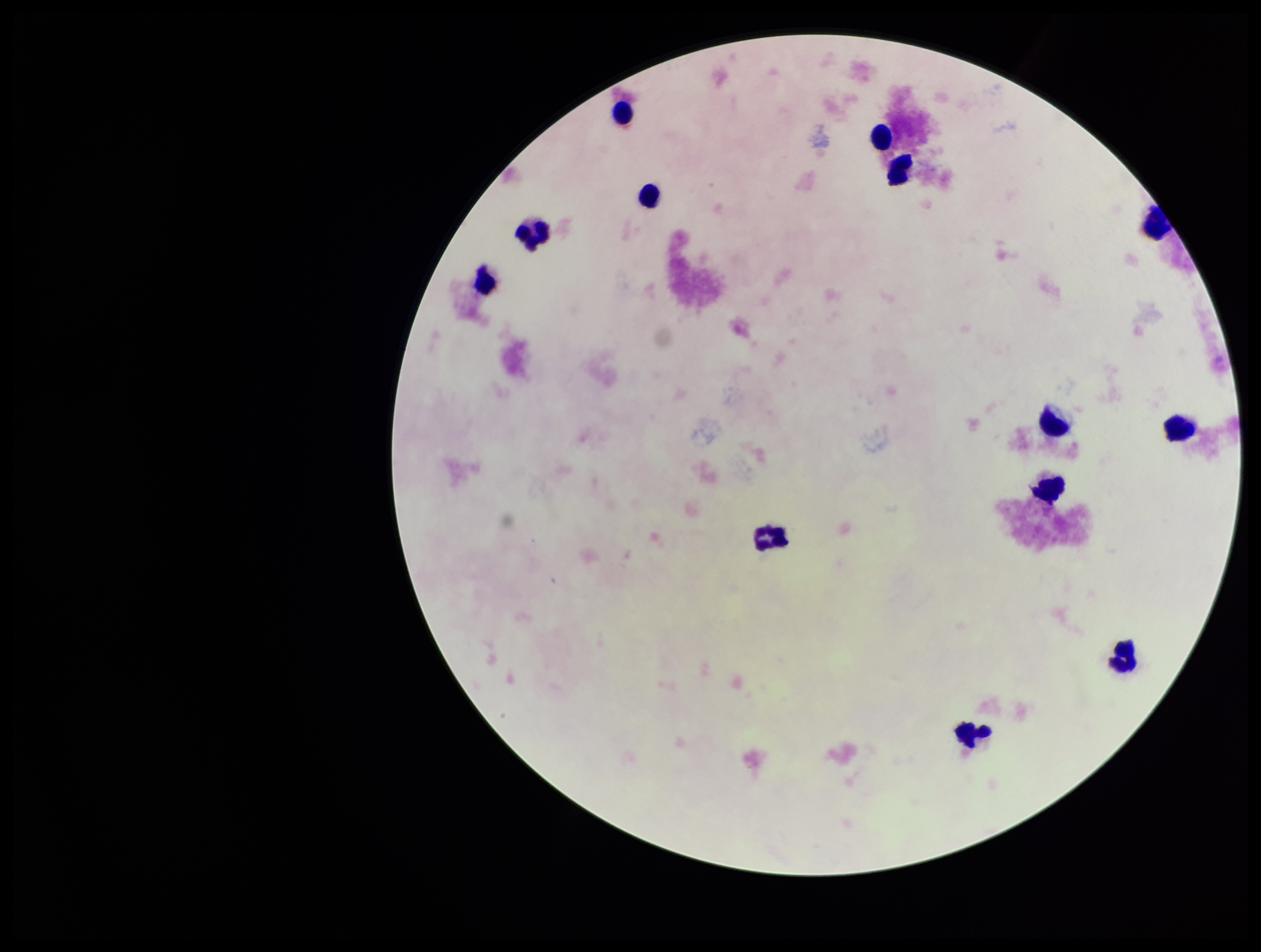
capture = smartphone photograph through the microscope eyepiece
patient malaria status = negative
field of view = one from this slide
Plasmodium parasites = none identified
stain = Giemsa
image size = 1261×952 pixels
preparation = thick
leukocyte count = 13
parasite count = 0